Point out Plasmodium parasites and leukocytes.
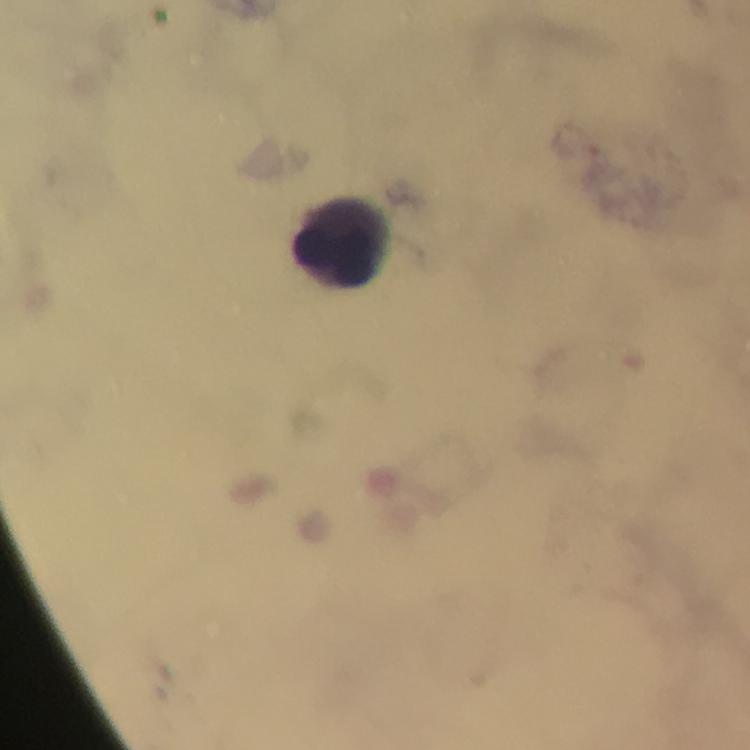
No Plasmodium parasites detected.
Approximate centers as {x, y} in pixels.
Leukocytes: {340, 244}.

immersion oil = applied
stain = Giemsa
capture = smartphone photograph through a microscope
cropped from = a single field of view
preparation = thick blood smear
image size = 750×750 pixels
context = from a diagnostic examination for malaria
magnification = 100x